Assess this cell for malaria.
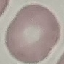
It is uninfected.

Summary:
  - Stain: Giemsa
  - Image type: automatically extracted cell patch, resized to 64 × 64 pixels
  - Preparation: thin smear
  - Capture: smartphone through the microscope eyepiece